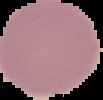

Summary:
  - Preparation: thin blood smear
  - Image size: 103×100 pixels
  - Image type: segmented cell region on a black background
  - Result: negative for Plasmodium parasites